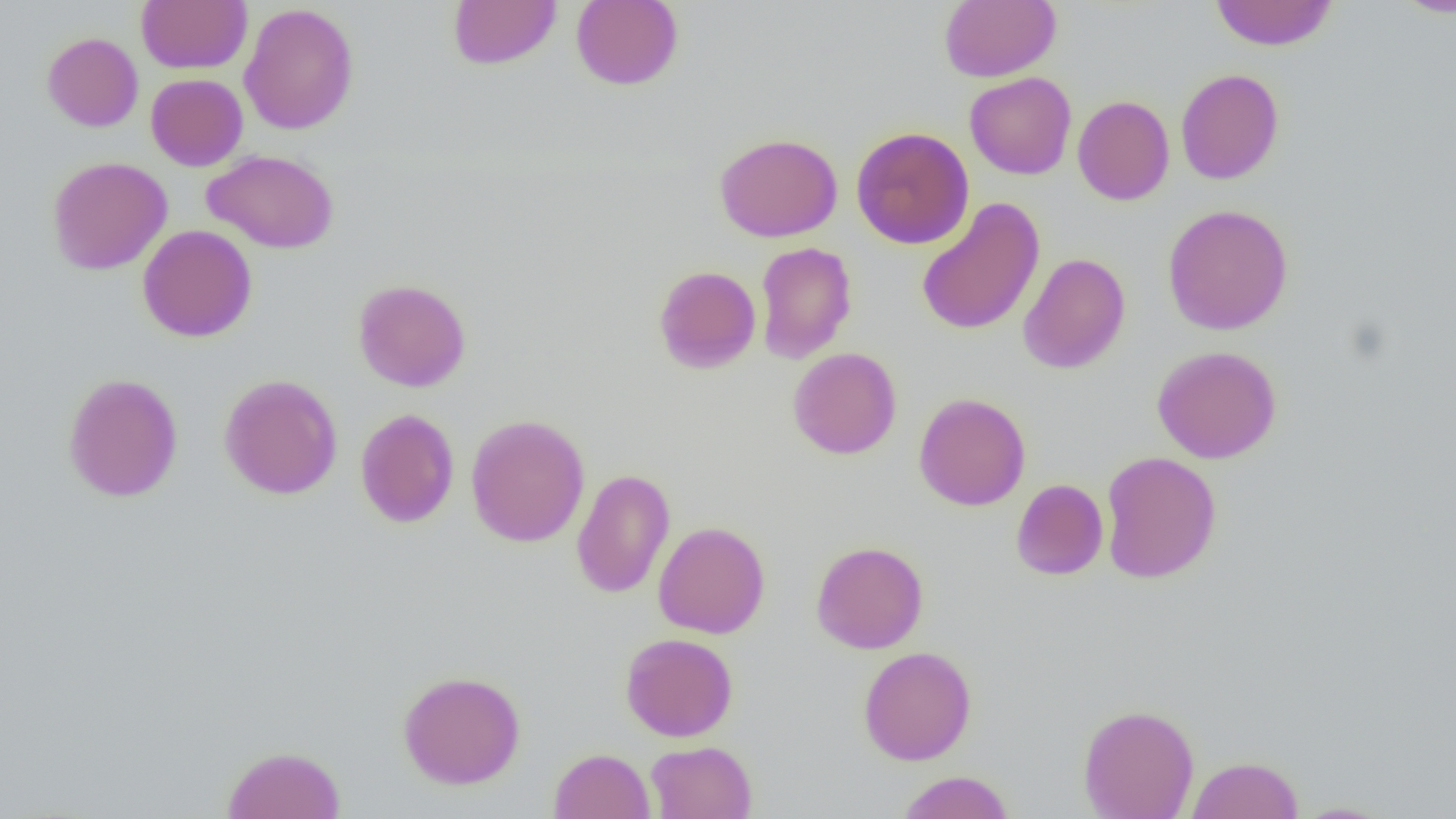 Approximate bounding boxes as [x1, y1, x2, y2] in pixels. Uninfected red blood cell locations: [448, 0, 561, 70], [571, 0, 684, 91], [939, 0, 1061, 82], [1393, 0, 1456, 18], [137, 1, 251, 73], [1209, 1, 1338, 51], [239, 3, 360, 135], [41, 32, 143, 132], [1175, 68, 1284, 185], [964, 72, 1077, 180], [146, 73, 248, 171], [1072, 95, 1175, 206], [850, 126, 974, 249], [714, 132, 843, 242], [202, 149, 339, 254], [47, 156, 172, 275], [916, 197, 1046, 336], [1162, 204, 1294, 335], [137, 224, 258, 342], [754, 241, 857, 364], [1018, 252, 1130, 374], [653, 265, 761, 374], [353, 278, 471, 392], [1151, 345, 1282, 463], [788, 347, 902, 460], [62, 372, 183, 503], [218, 373, 343, 500], [914, 392, 1031, 511], [355, 408, 460, 529], [465, 414, 590, 548], [1099, 451, 1222, 584], [571, 468, 676, 599], [1010, 478, 1109, 580], [653, 521, 770, 639], [811, 540, 928, 654], [620, 632, 738, 742], [858, 646, 977, 765], [397, 670, 526, 790], [1078, 703, 1199, 819], [644, 740, 757, 819], [222, 745, 346, 819], [549, 747, 654, 819], [1186, 755, 1304, 819], [895, 770, 1016, 819], [1289, 801, 1399, 818]. Slide-level diagnosis: negative for blood parasites. Thin blood smear. One field of a larger specimen. Captured at 1000x magnification. Light microscopy. Image is 1456×819 pixels.